Describe the morphology of the erythrocytes.
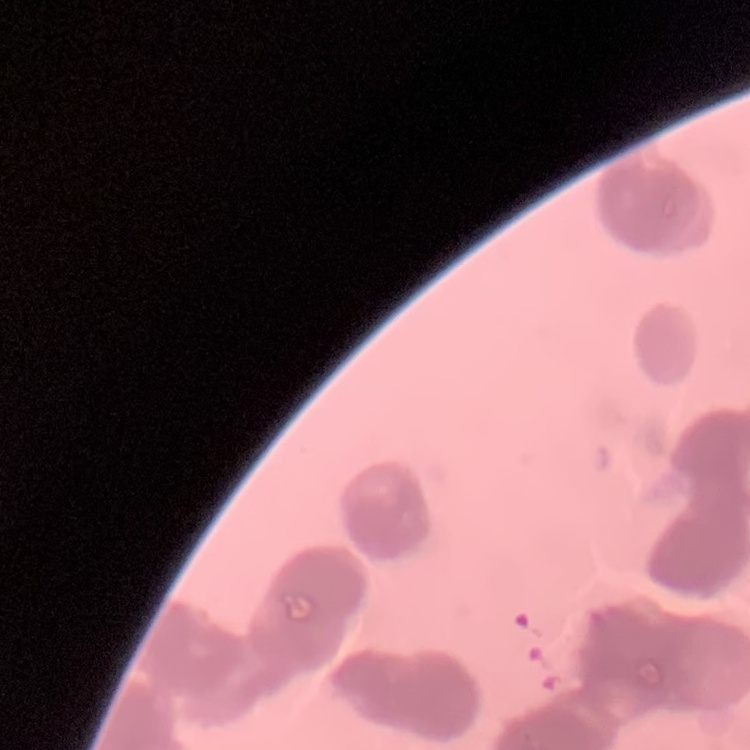
They show rouleaux formation.

Stained with either Field's or Giemsa. Thin blood smear. Square crop of a larger photomicrograph.